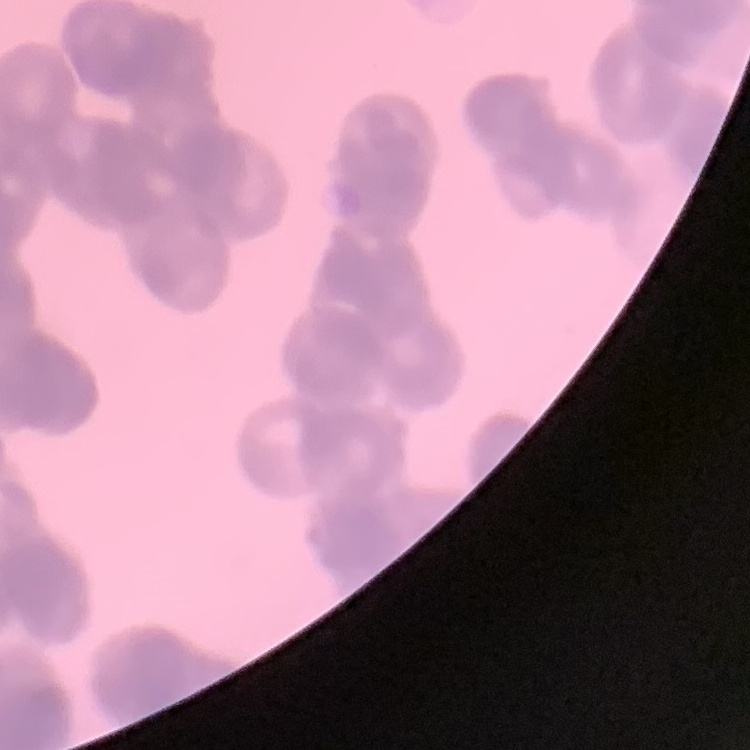
{
  "red_blood_cell_morphology": "rouleaux formation",
  "preparation": "thin peripheral smear",
  "stain": "Field's or Giemsa",
  "image_type": "one tile cut from a larger photomicrograph"
}